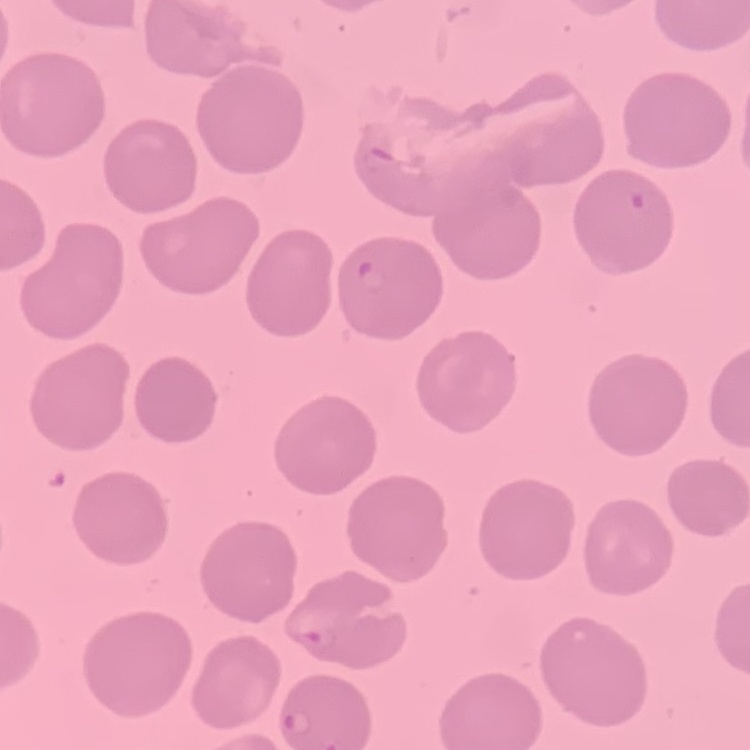

Summary:
  - Red blood cell morphology: no rouleaux formation
  - Preparation: thin peripheral smear
  - Image type: one tile cut from a larger photomicrograph
  - Stain: Field's or Giemsa